Classify the preparation.
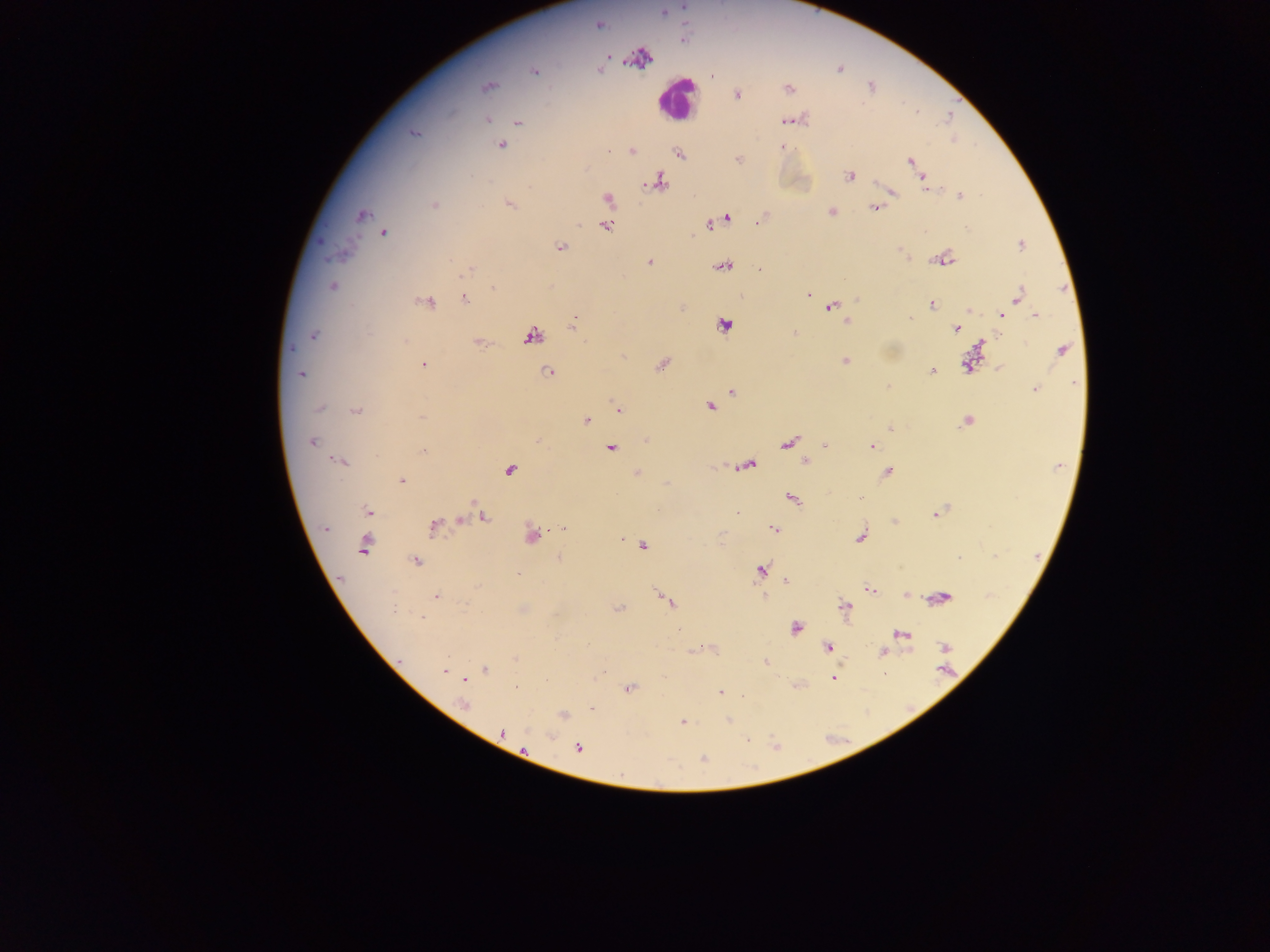

Thick blood smear.

{
  "malaria_parasite_locations": "approximate centers as [x, y] in pixels: [684, 5], [664, 12], [598, 24], [640, 59], [600, 70], [839, 70], [534, 71], [488, 86], [789, 88], [737, 95], [486, 119], [789, 120], [518, 123], [413, 133], [502, 146], [782, 147], [608, 150], [632, 151], [679, 155], [738, 159], [911, 161], [850, 176], [923, 180], [658, 183], [928, 188], [892, 193], [960, 196], [608, 199], [434, 205], [511, 206], [874, 208], [830, 212], [361, 215], [728, 218], [718, 221], [757, 221], [709, 224], [607, 226], [967, 228], [383, 233], [1020, 245], [560, 247], [902, 253], [946, 259], [650, 262], [723, 267], [760, 268], [467, 271], [333, 286], [493, 287], [809, 295], [1019, 295], [465, 300], [427, 303], [931, 305], [831, 306], [969, 309], [1002, 314], [1036, 315], [910, 319], [846, 321], [725, 325], [571, 326], [957, 328], [795, 334], [314, 336], [531, 337], [406, 340], [479, 342], [984, 344], [292, 348], [1062, 350], [623, 356], [845, 361], [662, 364], [424, 365], [967, 365], [1000, 368], [932, 371], [548, 372], [302, 374], [1075, 382], [1033, 389], [732, 391], [710, 406], [319, 407], [618, 409], [356, 412], [421, 417], [586, 420], [967, 421], [890, 429], [646, 441], [312, 442], [789, 443], [825, 446], [871, 446], [610, 449], [423, 452], [806, 461], [340, 462], [748, 465], [1058, 466], [509, 470], [637, 472], [888, 472], [402, 481], [792, 499], [367, 511], [737, 512], [935, 514], [482, 516], [433, 527], [326, 528], [563, 529], [773, 530], [531, 534], [861, 537], [363, 545], [643, 546], [558, 557], [959, 557], [415, 560], [760, 570], [518, 574], [786, 581], [870, 589], [436, 595], [907, 595], [764, 597], [943, 597], [666, 601], [844, 606], [618, 609], [394, 610], [422, 618], [796, 628], [678, 629], [901, 634], [828, 647], [945, 647], [694, 651], [883, 652], [516, 658], [766, 662], [485, 669], [945, 670], [444, 671], [834, 679], [464, 680], [516, 688], [629, 688], [721, 692], [464, 705], [592, 709], [563, 715], [728, 720], [682, 722], [502, 731], [550, 736], [747, 739], [578, 749], [523, 750], [702, 759]",
  "capture": "mobile-phone photograph through a microscope",
  "field_of_view": "single",
  "image_size": "1270×952 pixels",
  "country": "Ghana",
  "leukocyte_locations": "approximate centers as [x, y] in pixels: [674, 99]"
}